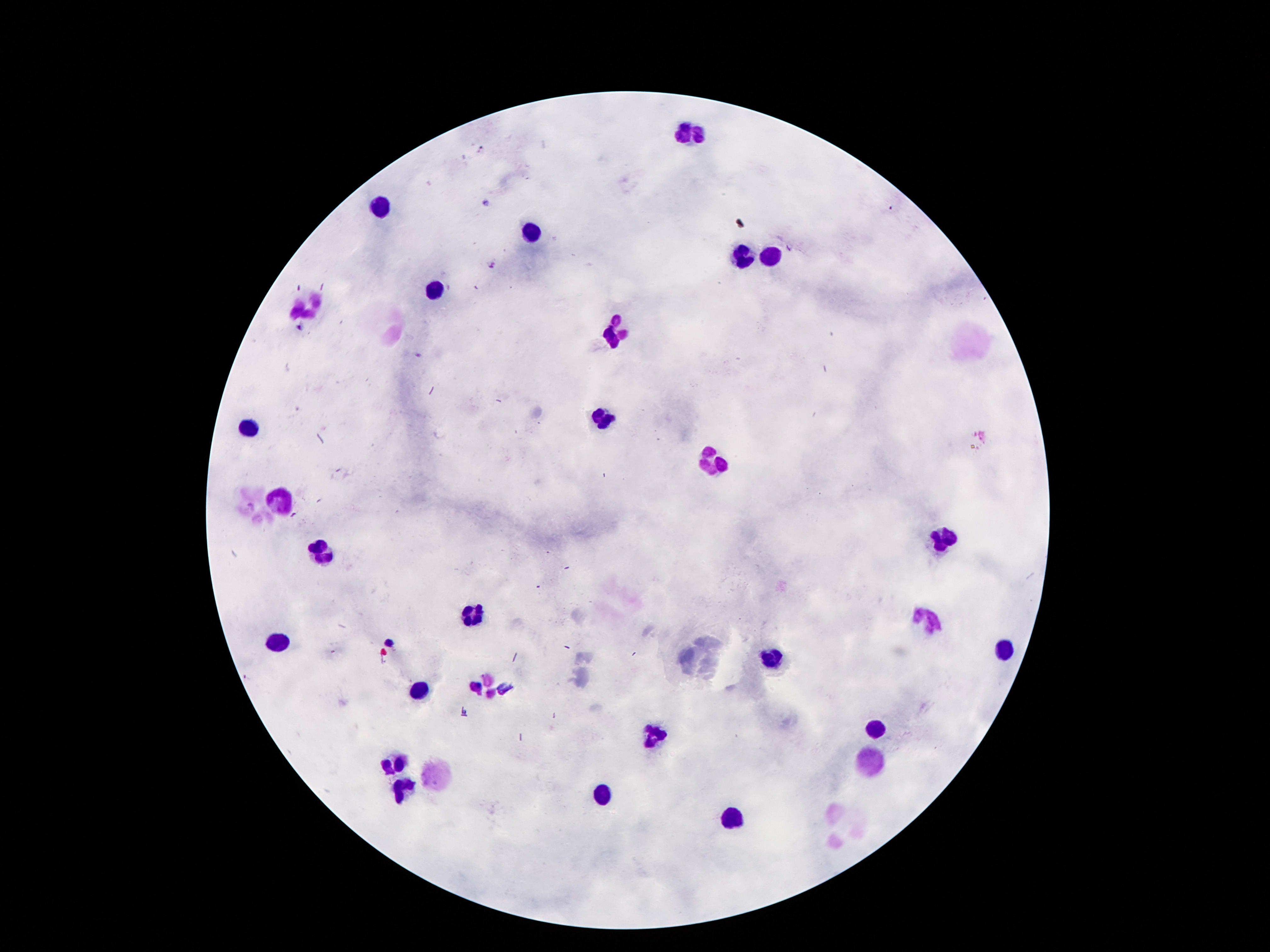
Approximate centers as {x, y} in pixels. Leukocyte locations: {691, 133}, {382, 207}, {530, 234}, {740, 255}, {777, 256}, {435, 291}, {306, 307}, {616, 333}, {600, 417}, {247, 428}, {715, 463}, {282, 497}, {941, 536}, {320, 549}, {474, 618}, {925, 619}, {275, 641}, {1005, 649}, {771, 660}, {490, 684}, {419, 689}, {877, 727}, {654, 736}, {393, 760}, {872, 763}, {437, 775}, {404, 793}, {603, 795}, {733, 818}. Photographed through the microscope eyepiece with a smartphone camera. One field from this slide. Image is 1270×952 pixels. 100x magnification. Patient malaria status: not infected. Giemsa-stained preparation. Thick blood smear.